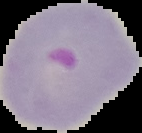

Malaria status: parasitized. Cell region segmented out of the field of view; the surrounding area is masked to black. Image is 142×133 pixels. From a thin blood smear.